Outline each Plasmodium ovale-infected red blood cell.
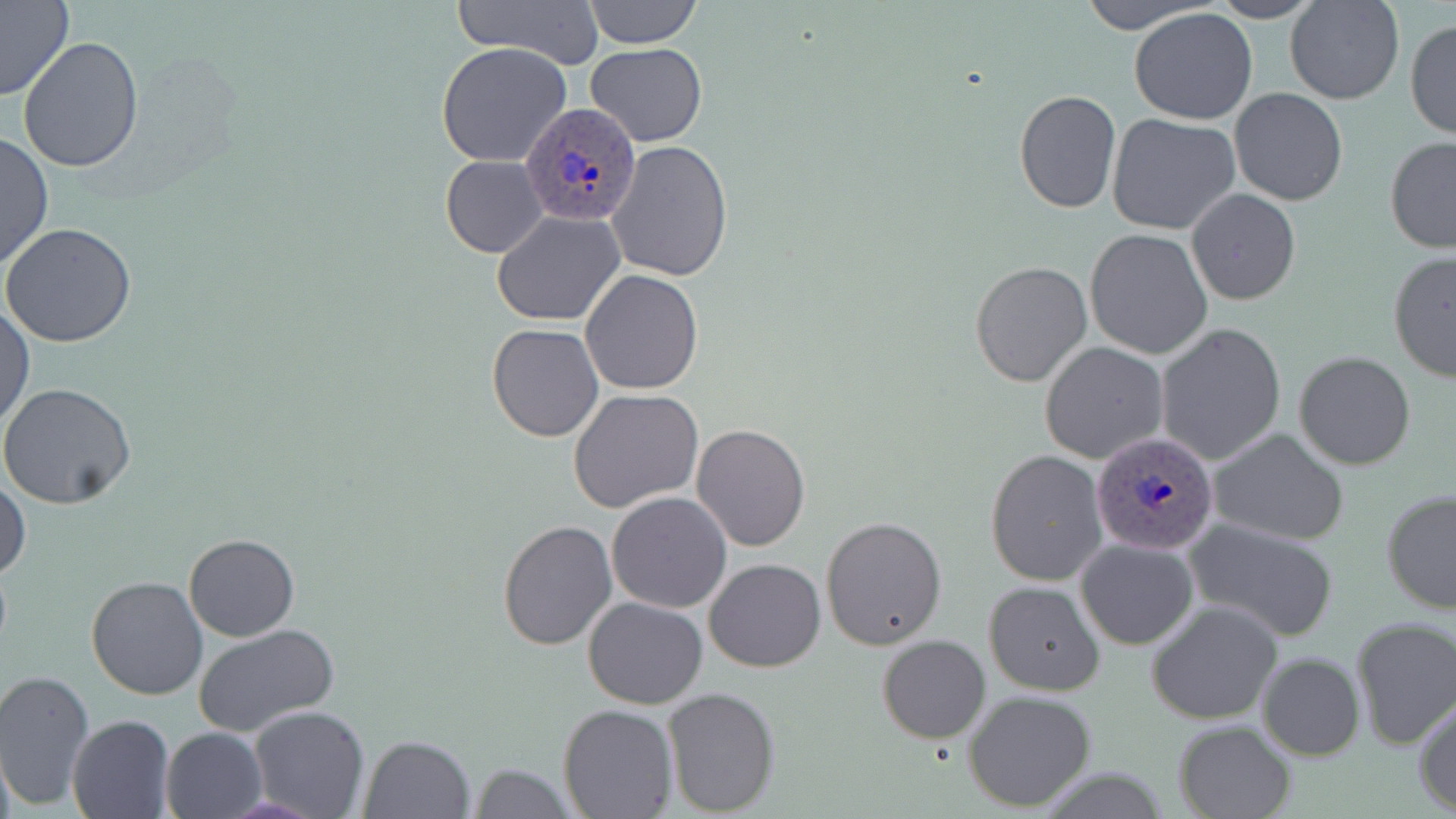
Approximate bounding boxes as (x1,y1)-(x2,y2) corner pairs in pixels.
Plasmodium ovale-infected red blood cells: (519,102)-(643,230), (1092,433)-(1218,555).

Summary:
  - Uninfected red blood cell locations: (0,0)-(77,102), (458,0)-(605,68), (582,0)-(703,49), (1074,0)-(1226,35), (1206,0)-(1328,23), (1284,0)-(1403,104), (1129,8)-(1260,126), (1405,19)-(1456,141), (18,37)-(145,174), (585,42)-(709,146), (436,43)-(575,167), (1230,88)-(1347,206), (1014,90)-(1121,213), (1107,114)-(1242,237), (0,131)-(53,272), (1384,136)-(1456,254), (605,139)-(734,283), (440,155)-(548,258), (1185,189)-(1301,307), (493,210)-(625,327), (2,223)-(137,348), (1085,227)-(1215,361), (1387,249)-(1456,382), (969,261)-(1092,386), (580,269)-(705,394), (0,303)-(35,430), (486,323)-(604,442), (1154,324)-(1289,469), (1039,341)-(1167,464), (1294,351)-(1417,471), (0,382)-(136,509), (569,388)-(704,514), (691,423)-(812,552), (1207,428)-(1352,546), (986,449)-(1108,588), (1,478)-(31,582), (1380,488)-(1456,613), (605,492)-(732,613), (820,516)-(948,651), (497,518)-(615,650), (1184,519)-(1340,642), (183,533)-(301,641), (1075,538)-(1199,652), (704,558)-(826,672), (85,574)-(208,700), (983,580)-(1105,695), (583,596)-(708,709), (1146,600)-(1282,725), (1350,617)-(1456,750), (191,623)-(338,737), (876,634)-(990,743), (1257,652)-(1364,761), (0,669)-(96,809), (663,687)-(780,814), (963,689)-(1097,811), (1414,697)-(1456,816), (559,704)-(677,818), (247,707)-(371,819), (66,714)-(175,818), (1171,719)-(1295,819), (160,727)-(266,819), (358,733)-(475,818), (466,761)-(577,818)
  - Slide-level diagnosis: Plasmodium ovale
  - Preparation: thin blood film
  - Image size: 1456×819 pixels
  - Modality: light microscopy
  - Field of view: single
  - Stain: May-Grünwald-Giemsa
  - Magnification: 1000x